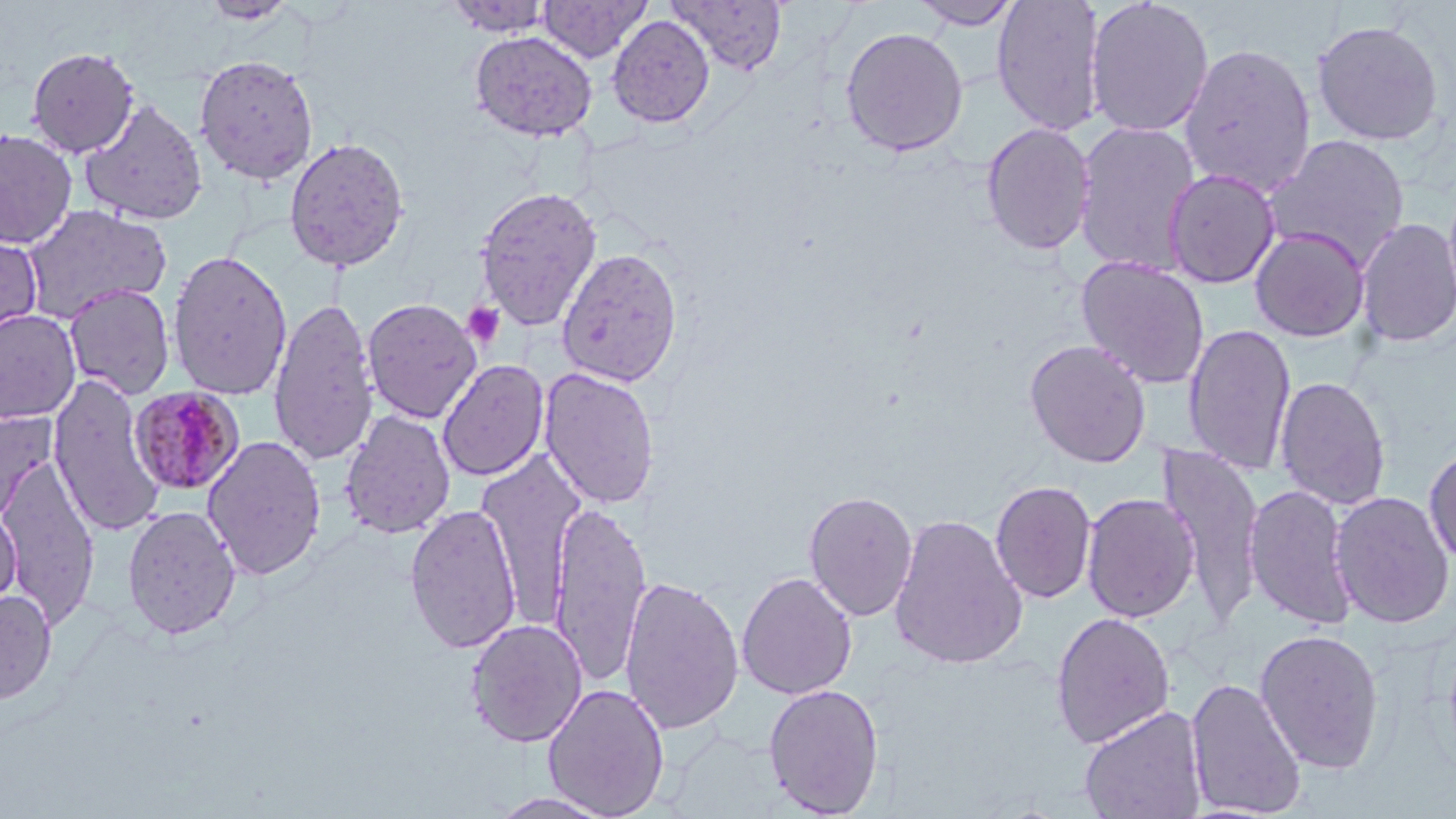 Approximate bounding boxes as (x1,y1)-(x2,y2) corner pairs in pixels. Uninfected red blood cell locations: (444,0)-(556,37), (538,0)-(652,62), (669,0)-(788,75), (910,0)-(1022,30), (991,0)-(1106,136), (1084,0)-(1215,137), (607,14)-(715,128), (1311,19)-(1445,146), (839,26)-(968,158), (469,30)-(598,142), (1178,42)-(1317,198), (26,46)-(140,158), (193,54)-(320,185), (80,99)-(208,226), (1073,119)-(1202,277), (980,122)-(1096,255), (0,128)-(78,249), (1265,134)-(1411,269), (282,135)-(410,273), (1163,168)-(1281,288), (474,186)-(603,331), (20,204)-(173,322), (1355,217)-(1456,348), (1250,227)-(1371,342), (0,229)-(44,350), (556,247)-(684,388), (167,249)-(293,401), (1075,256)-(1210,389), (63,284)-(176,400), (268,296)-(379,466), (361,298)-(483,423), (0,309)-(82,425), (1183,323)-(1297,477), (1024,339)-(1152,468), (437,359)-(549,481), (539,366)-(660,509), (47,374)-(166,539), (1275,375)-(1391,511), (0,407)-(58,526), (339,409)-(457,540), (202,435)-(327,580), (1423,443)-(1456,567), (1158,444)-(1265,623), (477,450)-(585,627), (0,454)-(101,629), (989,479)-(1097,604), (1244,483)-(1359,630), (803,489)-(918,622), (1330,490)-(1454,629), (1081,492)-(1200,623), (549,500)-(652,687), (404,503)-(522,654), (0,504)-(21,612), (121,505)-(241,640), (888,513)-(1029,670), (736,571)-(857,700), (619,574)-(744,735), (0,589)-(57,704), (1050,611)-(1176,749), (465,619)-(587,747), (1254,628)-(1385,774), (1185,676)-(1307,818), (543,683)-(670,818), (763,683)-(885,817), (1079,706)-(1208,819), (487,791)-(617,818). Platelet locations: (462,302)-(505,348). Plasmodium malariae-infected red blood cell locations: (129,386)-(245,496). Slide-level diagnosis: Plasmodium malariae. May-Grünwald-Giemsa-stained preparation. Image is 1456×819 pixels. Captured at 1000x magnification. Light microscopy. Thin blood smear. One field of a larger specimen.